Assess this cell for malaria.
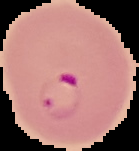

It is parasitized.

Image is 139×151 pixels. The area outside the segmented cell region is set to black. From a thin blood film.